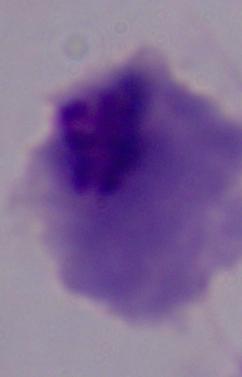

{
  "modality": "micrograph",
  "magnification": "1000x",
  "identification": "trichomonad"
}